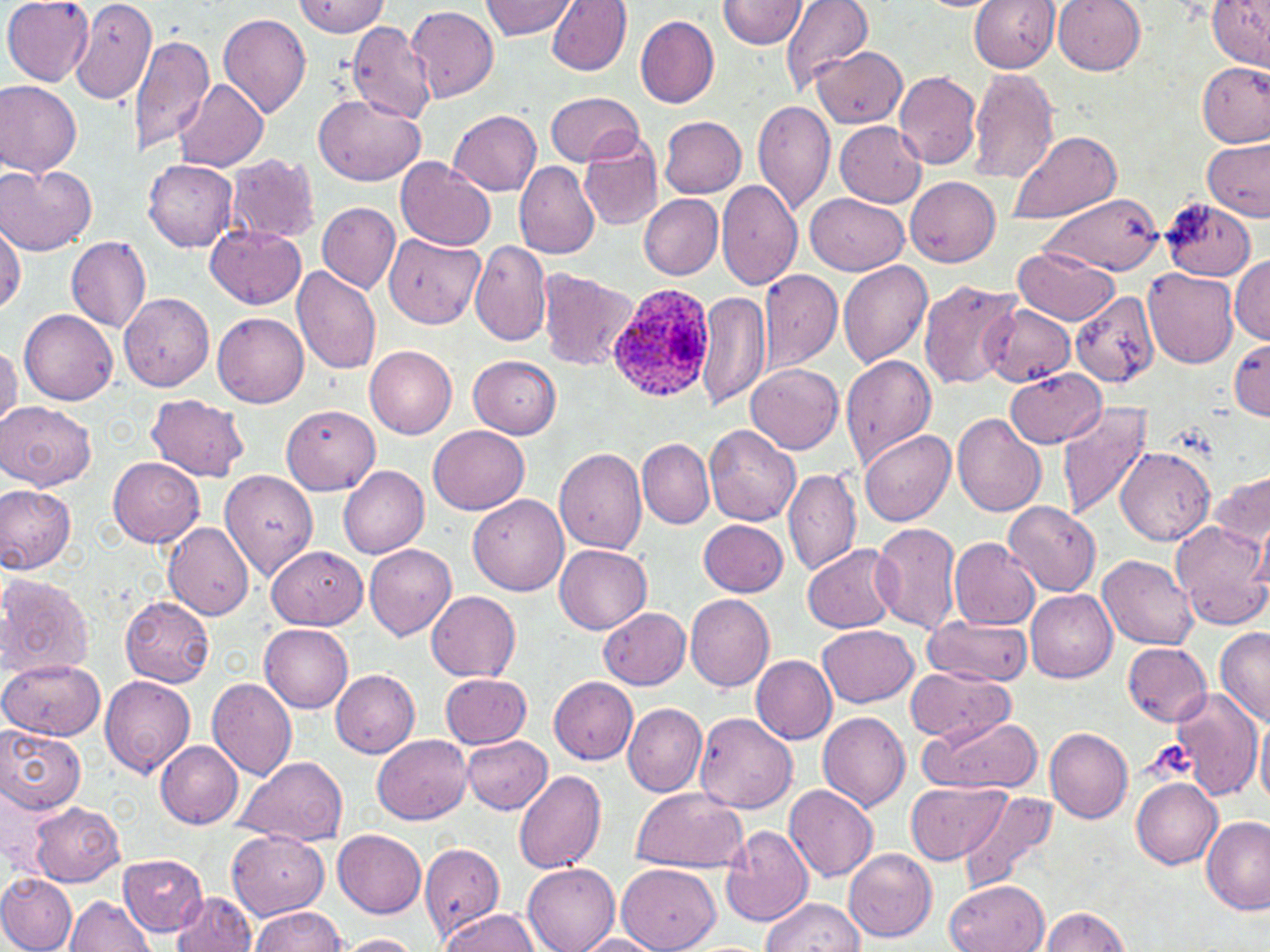

Summary:
  - Coordinate format: approximate bounding boxes as [x1, y1, x2, y2] in pixels
  - Uninfected red blood cell locations: [2, 0, 95, 85], [68, 0, 158, 105], [480, 0, 577, 40], [547, 0, 632, 75], [779, 0, 873, 96], [969, 0, 1060, 73], [1053, 0, 1146, 75], [1207, 0, 1270, 69], [293, 1, 389, 37], [719, 1, 810, 49], [408, 4, 499, 104], [635, 12, 719, 108], [217, 13, 311, 118], [347, 22, 437, 123], [130, 33, 214, 158], [811, 46, 907, 129], [1199, 61, 1268, 148], [968, 68, 1060, 185], [892, 72, 982, 170], [175, 79, 268, 174], [0, 81, 82, 177], [314, 93, 428, 185], [545, 93, 645, 168], [753, 98, 835, 216], [450, 110, 542, 195], [659, 116, 747, 198], [835, 122, 926, 207], [1009, 129, 1120, 225], [580, 135, 664, 230], [1202, 137, 1270, 222], [227, 154, 320, 243], [144, 159, 238, 251], [396, 159, 495, 252], [515, 161, 601, 259], [1, 165, 95, 254], [905, 174, 1001, 266], [716, 178, 802, 291], [806, 192, 908, 276], [639, 195, 723, 279], [1040, 195, 1163, 275], [1162, 198, 1258, 283], [317, 202, 400, 292], [0, 218, 25, 315], [206, 226, 305, 310], [383, 235, 484, 327], [66, 237, 151, 333], [470, 242, 553, 347], [1011, 249, 1120, 324], [1231, 254, 1270, 344], [838, 259, 932, 369], [290, 268, 383, 376], [1144, 269, 1239, 368], [758, 270, 843, 371], [539, 271, 639, 372], [918, 279, 1021, 389], [696, 290, 771, 413], [1071, 291, 1163, 388], [120, 293, 214, 391], [979, 303, 1077, 387], [20, 309, 118, 405], [213, 312, 309, 408], [1229, 338, 1269, 420], [0, 343, 19, 429], [364, 344, 458, 439], [841, 354, 937, 467], [469, 355, 562, 439], [745, 362, 843, 453], [1007, 368, 1105, 448], [146, 394, 249, 482], [1053, 401, 1153, 521], [1, 402, 97, 490], [282, 405, 379, 494], [951, 412, 1048, 517], [704, 425, 801, 527], [428, 426, 529, 516], [860, 429, 956, 527], [637, 439, 715, 527], [553, 447, 648, 554], [1115, 447, 1216, 546], [107, 457, 204, 548], [221, 465, 320, 581], [338, 465, 430, 558], [784, 467, 861, 577], [1210, 468, 1270, 559], [0, 484, 76, 574], [467, 494, 568, 596], [1001, 500, 1101, 595], [1252, 512, 1270, 593], [698, 519, 788, 597], [870, 520, 962, 634], [1170, 520, 1269, 630], [163, 523, 254, 620], [949, 537, 1039, 630], [364, 544, 456, 641], [555, 544, 651, 634], [802, 544, 900, 634], [267, 546, 368, 629], [1098, 555, 1198, 648], [0, 572, 94, 681], [1025, 589, 1117, 683], [426, 591, 522, 681], [685, 594, 775, 692], [120, 597, 216, 688], [598, 606, 692, 689], [920, 616, 1033, 687], [260, 624, 354, 712], [817, 625, 918, 705], [1214, 627, 1269, 725], [1123, 643, 1213, 727], [751, 656, 838, 744], [1, 659, 104, 740], [904, 667, 1015, 744], [330, 670, 419, 756], [440, 671, 532, 749], [100, 674, 196, 777], [206, 677, 298, 782], [549, 677, 637, 764], [1167, 686, 1263, 799], [622, 702, 707, 797], [1255, 711, 1270, 809], [817, 712, 910, 813], [694, 713, 798, 814], [919, 715, 1043, 794], [1045, 725, 1133, 823], [0, 726, 86, 813], [460, 734, 552, 814], [374, 735, 472, 824], [155, 742, 244, 829], [234, 755, 349, 847], [514, 767, 607, 874], [1131, 777, 1224, 868], [905, 779, 1012, 864], [785, 785, 878, 882], [630, 788, 748, 874], [958, 789, 1061, 892], [29, 801, 125, 886], [1202, 814, 1269, 916], [722, 826, 815, 928], [334, 829, 426, 918], [226, 831, 330, 922], [418, 843, 505, 937], [843, 848, 938, 943], [119, 854, 208, 937], [523, 863, 619, 952], [618, 864, 720, 952], [0, 874, 77, 952], [945, 879, 1049, 952], [171, 891, 258, 952], [63, 896, 154, 952], [760, 896, 865, 952], [1039, 906, 1132, 952], [249, 907, 345, 951], [439, 909, 542, 951], [333, 934, 422, 951], [571, 934, 665, 952]
  - Plasmodium ovale-infected red blood cell locations: [604, 280, 715, 402]
  - Slide-level diagnosis: Plasmodium ovale
  - Magnification: 1000x
  - Image size: 1270×952 pixels
  - Modality: optical microscopy
  - Stain: May-Grünwald-Giemsa
  - Preparation: thin blood smear
  - Field of view: one of a larger specimen